Point out each leukocyte.
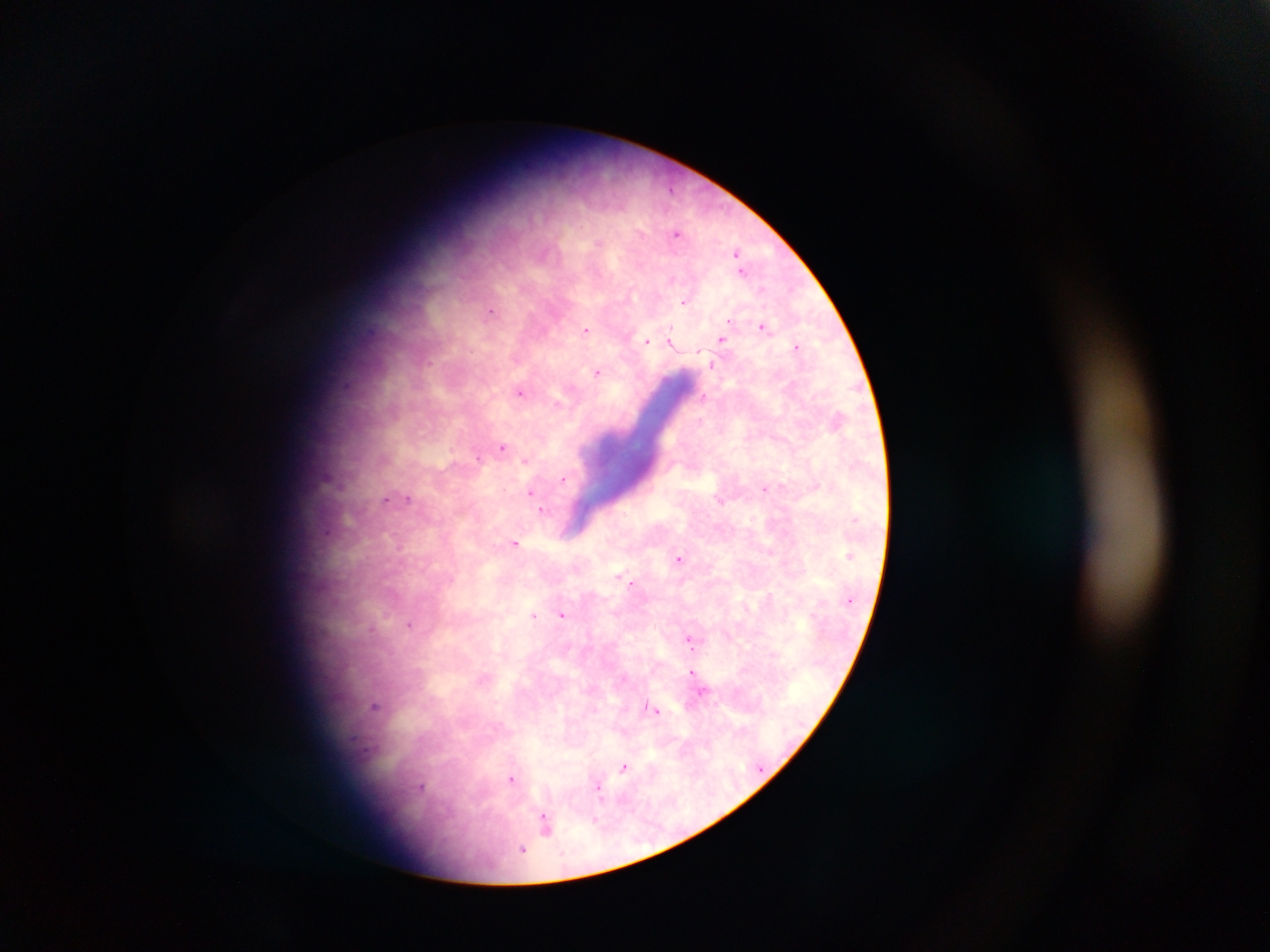

No leukocytes observed.

malaria parasite locations = approximate centers as (x, y) in pixels: (670, 189), (676, 233), (598, 242), (737, 253), (742, 271), (671, 278), (762, 288), (685, 301), (490, 312), (729, 321), (762, 326), (585, 330), (671, 339), (722, 339), (647, 340), (796, 346), (429, 362), (713, 365), (597, 372), (520, 392), (704, 397), (502, 447), (478, 457), (525, 461), (562, 479), (765, 489), (530, 493), (408, 497), (386, 499), (720, 500), (542, 511), (515, 543), (679, 558), (620, 575), (631, 582), (770, 595), (534, 615), (563, 615), (410, 624), (372, 629), (689, 639), (692, 673), (701, 692), (374, 706), (656, 711), (624, 767), (511, 779), (421, 786), (599, 791), (595, 820), (545, 824), (523, 849)
preparation = thick blood film
field of view = single
image size = 1270×952 pixels
country = Ghana
capture = mobile-phone photograph through a microscope